State which parasite is depicted.
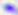

This is Toxoplasma gondii.

modality = photomicrograph
magnification = 400x